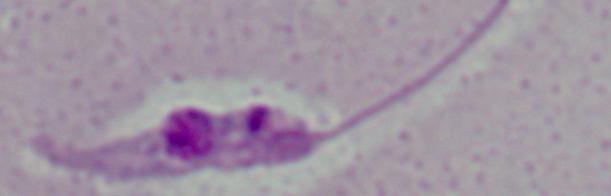

Summary:
  - Magnification: 1000x
  - Identification: Leishmania
  - Modality: photomicrograph